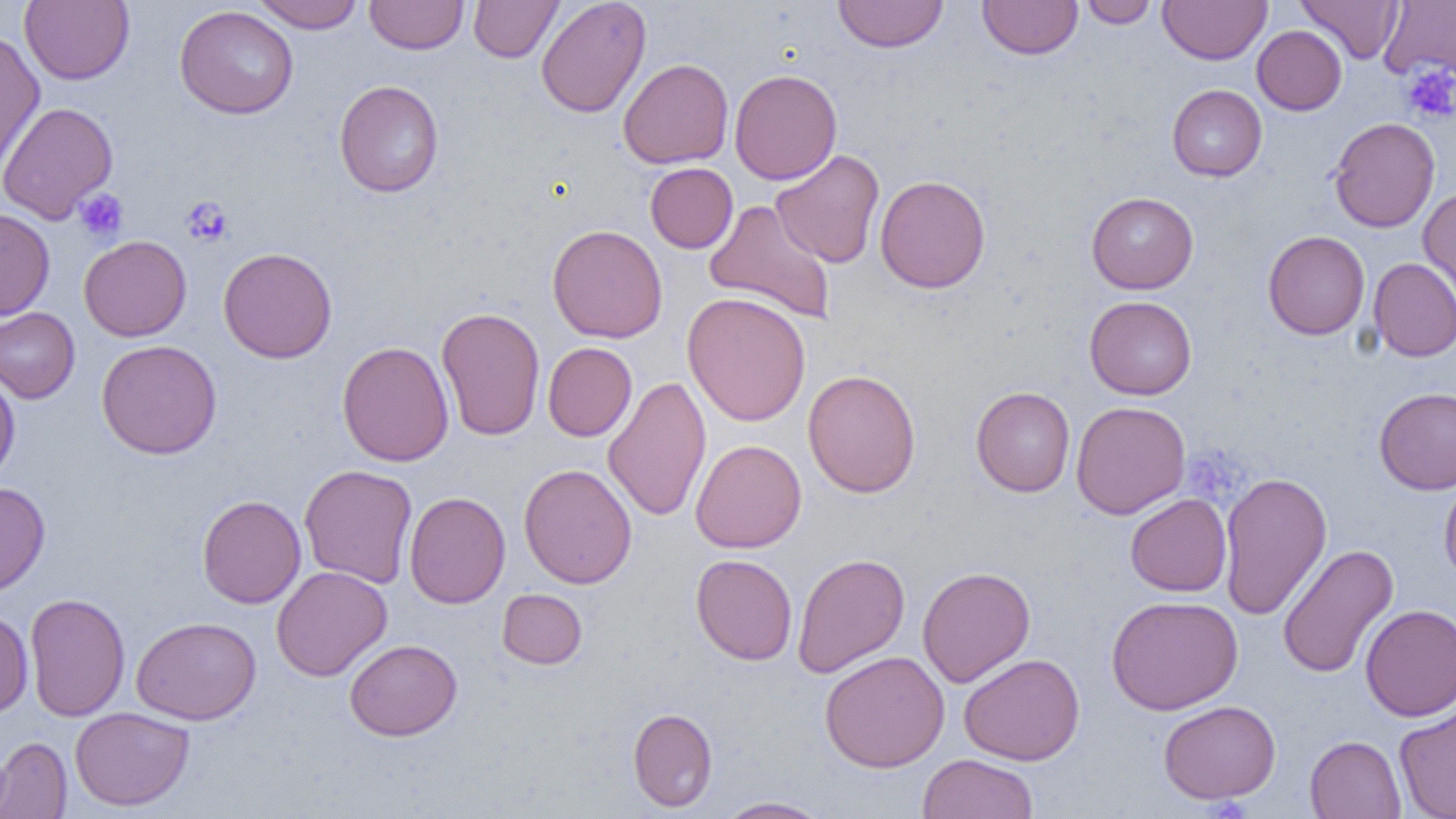 Approximate bounding boxes as (x1,y1)-(x2,y2) corner pairs in pixels. Platelet locations: (1401,63)-(1456,124), (74,189)-(128,241), (180,196)-(233,247), (1189,446)-(1259,503). Uninfected red blood cell locations: (20,0)-(134,85), (249,0)-(365,33), (365,0)-(468,54), (468,0)-(563,63), (536,0)-(651,118), (833,0)-(948,53), (977,0)-(1083,60), (1079,0)-(1158,28), (1158,0)-(1271,65), (1296,0)-(1404,64), (1379,0)-(1456,80), (174,5)-(299,119), (1252,25)-(1347,115), (0,29)-(45,177), (618,58)-(733,169), (729,69)-(842,185), (334,80)-(444,198), (1167,85)-(1267,181), (0,101)-(117,224), (1328,116)-(1441,233), (770,149)-(885,268), (645,162)-(738,253), (875,174)-(990,293), (1418,187)-(1456,310), (1086,192)-(1199,294), (703,199)-(837,324), (0,208)-(55,320), (547,224)-(668,343), (1262,230)-(1370,340), (78,235)-(192,341), (218,247)-(336,363), (1368,257)-(1456,362), (682,292)-(811,426), (1084,296)-(1197,399), (0,307)-(80,403), (436,307)-(546,441), (96,339)-(222,460), (337,340)-(454,467), (542,342)-(637,441), (803,369)-(921,498), (0,372)-(20,484), (602,375)-(712,523), (971,386)-(1075,497), (1374,386)-(1456,495), (1071,401)-(1191,519), (690,439)-(806,554), (299,464)-(418,588), (519,464)-(637,589), (1218,472)-(1332,621), (1439,475)-(1456,588), (0,481)-(50,597), (404,491)-(510,608), (1125,493)-(1231,597), (197,494)-(306,608), (1277,544)-(1398,679), (791,552)-(910,678), (691,554)-(797,665), (271,565)-(392,681), (917,566)-(1035,687), (497,588)-(587,669), (24,593)-(130,721), (1105,595)-(1243,715), (1360,604)-(1456,720), (0,608)-(33,718), (131,616)-(261,725), (343,638)-(462,741), (819,650)-(950,773), (959,653)-(1085,766), (1394,698)-(1456,819), (1158,700)-(1281,804), (69,707)-(195,811), (627,707)-(718,812), (1305,735)-(1406,818), (0,736)-(72,818), (918,753)-(1039,819), (713,796)-(832,818). Slide-level diagnosis: negative for blood parasites. Optical microscopy. 1000x magnification. Single field of view. Thin blood smear. Image is 1456×819 pixels.